Name the blood parasite species.
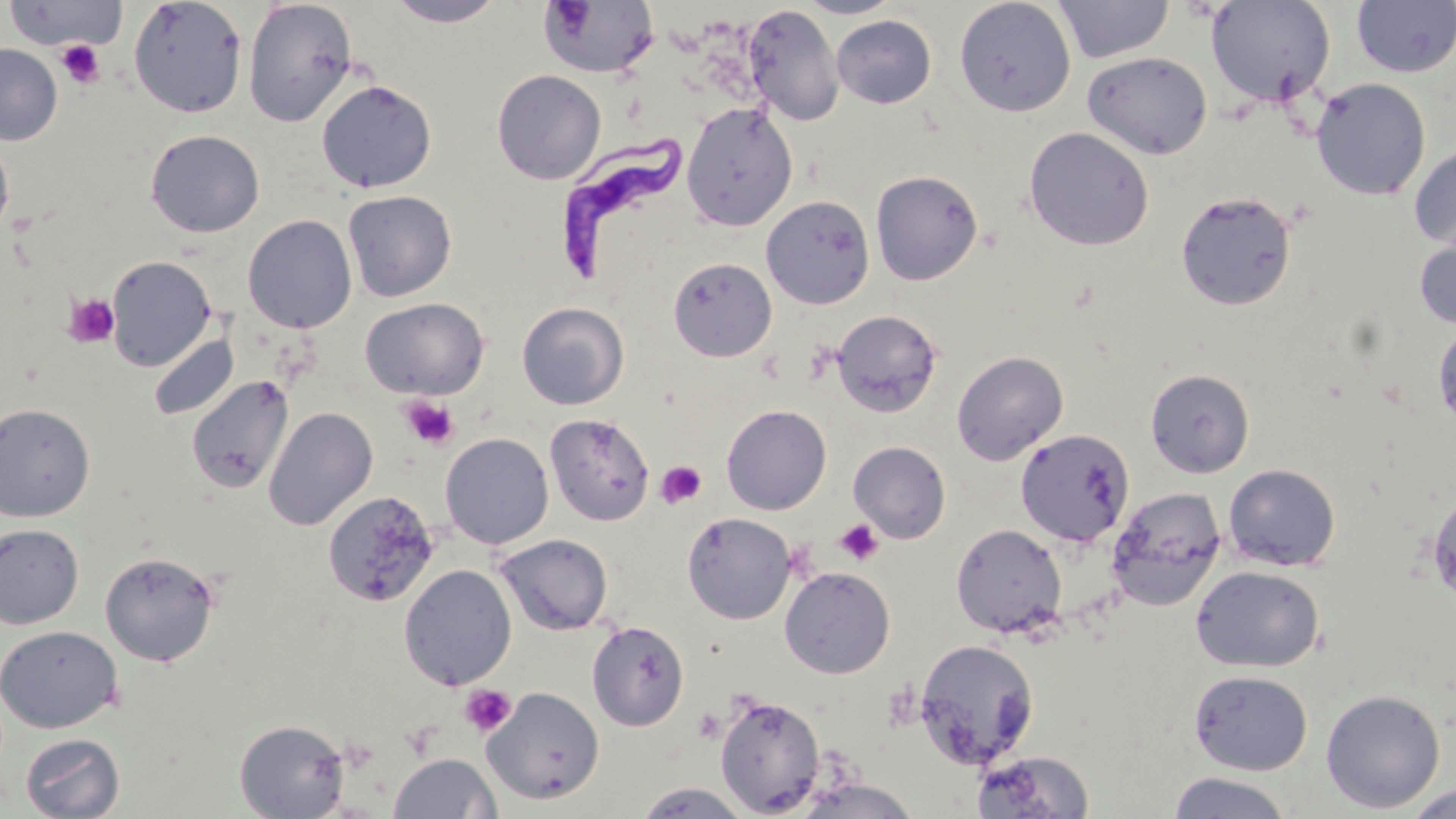
Trypanosoma brucei.

preparation = thin blood film
image size = 1456×819 pixels
platelet locations = approximate bounding boxes as named x1/y1/x2/y2 corners in pixels: (x1=55, y1=39, x2=106, y2=89), (x1=63, y1=292, x2=120, y2=348), (x1=399, y1=396, x2=459, y2=450), (x1=655, y1=459, x2=707, y2=510), (x1=835, y1=519, x2=883, y2=566), (x1=459, y1=684, x2=517, y2=737)
uninfected red blood cell locations = approximate bounding boxes as named x1/y1/x2/y2 corners in pixels: (x1=127, y1=0, x2=248, y2=118), (x1=796, y1=0, x2=904, y2=18), (x1=1055, y1=0, x2=1172, y2=63), (x1=1206, y1=0, x2=1336, y2=109), (x1=2, y1=1, x2=127, y2=51), (x1=242, y1=1, x2=359, y2=127), (x1=385, y1=1, x2=507, y2=27), (x1=537, y1=1, x2=659, y2=79), (x1=954, y1=1, x2=1076, y2=116), (x1=1351, y1=1, x2=1455, y2=78), (x1=743, y1=6, x2=844, y2=126), (x1=831, y1=15, x2=937, y2=108), (x1=0, y1=44, x2=63, y2=145), (x1=1082, y1=51, x2=1212, y2=160), (x1=492, y1=69, x2=607, y2=185), (x1=316, y1=78, x2=437, y2=192), (x1=1311, y1=78, x2=1431, y2=200), (x1=681, y1=102, x2=798, y2=230), (x1=1023, y1=126, x2=1155, y2=251), (x1=145, y1=129, x2=265, y2=237), (x1=0, y1=134, x2=15, y2=238), (x1=1408, y1=145, x2=1456, y2=250), (x1=870, y1=169, x2=983, y2=285), (x1=343, y1=190, x2=458, y2=302), (x1=1176, y1=190, x2=1297, y2=310), (x1=761, y1=195, x2=875, y2=309), (x1=242, y1=214, x2=357, y2=333), (x1=1414, y1=232, x2=1456, y2=330), (x1=105, y1=255, x2=217, y2=371), (x1=668, y1=256, x2=777, y2=361), (x1=360, y1=297, x2=489, y2=400), (x1=517, y1=302, x2=629, y2=410), (x1=831, y1=308, x2=943, y2=417), (x1=1432, y1=321, x2=1456, y2=430), (x1=148, y1=332, x2=239, y2=421), (x1=952, y1=350, x2=1069, y2=465), (x1=1145, y1=368, x2=1255, y2=477), (x1=186, y1=374, x2=294, y2=495), (x1=0, y1=403, x2=95, y2=522), (x1=721, y1=404, x2=831, y2=515), (x1=263, y1=406, x2=378, y2=530), (x1=545, y1=414, x2=655, y2=525), (x1=1015, y1=428, x2=1135, y2=547), (x1=440, y1=432, x2=554, y2=549), (x1=848, y1=441, x2=950, y2=543), (x1=1223, y1=463, x2=1341, y2=572), (x1=1108, y1=486, x2=1226, y2=610), (x1=1427, y1=489, x2=1456, y2=602), (x1=322, y1=490, x2=441, y2=610), (x1=682, y1=511, x2=796, y2=624), (x1=0, y1=523, x2=84, y2=630), (x1=950, y1=523, x2=1067, y2=638), (x1=495, y1=533, x2=613, y2=635), (x1=100, y1=550, x2=220, y2=667), (x1=399, y1=563, x2=517, y2=690), (x1=1190, y1=564, x2=1324, y2=672), (x1=779, y1=566, x2=895, y2=678), (x1=587, y1=620, x2=690, y2=731), (x1=0, y1=624, x2=123, y2=733), (x1=914, y1=639, x2=1039, y2=768), (x1=1188, y1=669, x2=1313, y2=776), (x1=482, y1=686, x2=604, y2=804), (x1=1320, y1=689, x2=1446, y2=813), (x1=714, y1=692, x2=825, y2=816), (x1=234, y1=719, x2=350, y2=818), (x1=20, y1=732, x2=125, y2=818), (x1=970, y1=750, x2=1096, y2=818), (x1=388, y1=752, x2=502, y2=818), (x1=1167, y1=771, x2=1293, y2=818), (x1=790, y1=776, x2=926, y2=819), (x1=631, y1=782, x2=756, y2=819), (x1=1403, y1=783, x2=1456, y2=817)
field of view = single
Trypanosoma brucei locations = approximate bounding boxes as named x1/y1/x2/y2 corners in pixels: (x1=559, y1=127, x2=685, y2=286)
magnification = 1000x
modality = light microscopy
stain = May-Grünwald-Giemsa